Identify the parasite.
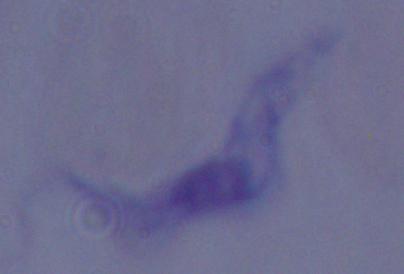

This is a trypanosome.

Photomicrograph. 1000x magnification.